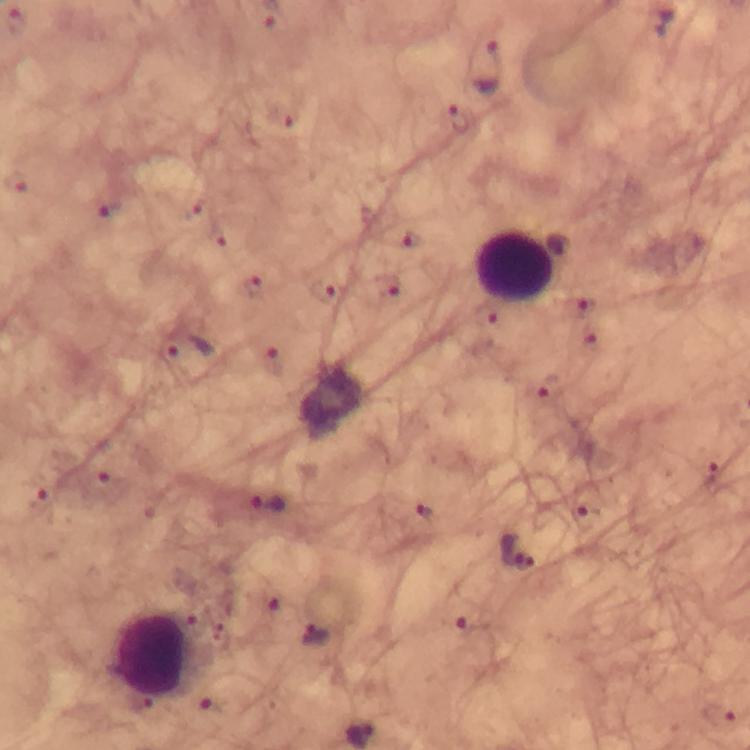

Approximate centers as {x, y} in pixels.
Summary:
  - Plasmodium parasite locations: {16, 21}, {276, 26}, {488, 68}, {285, 116}, {457, 118}, {105, 207}, {193, 207}, {217, 236}, {413, 243}, {254, 286}, {385, 286}, {321, 294}, {580, 307}, {485, 314}, {588, 339}, {189, 348}, {273, 361}, {542, 389}, {711, 474}, {107, 486}, {39, 495}, {271, 504}, {586, 513}, {424, 514}, {518, 551}, {269, 599}, {194, 620}, {468, 622}, {313, 633}, {214, 704}, {719, 714}
  - Leukocyte locations: {514, 268}, {155, 657}
  - Image size: 750×750 pixels
  - Immersion oil: applied
  - Capture: smartphone camera through the microscope
  - Stain: Giemsa
  - Context: from a diagnostic examination for malaria
  - Preparation: thick blood smear
  - Cropped from: one field of view
  - Magnification: 100x